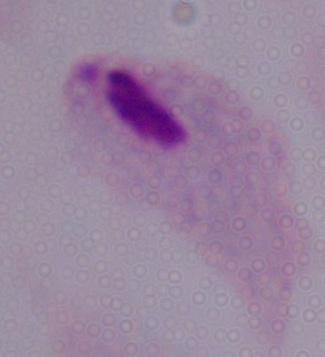
magnification = 1000x
identification = trichomonad
modality = photomicrograph